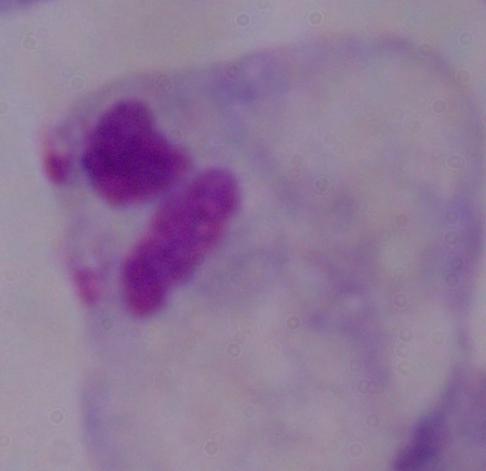
Photomicrograph. Captured at 1000x magnification. A trichomonad is shown.